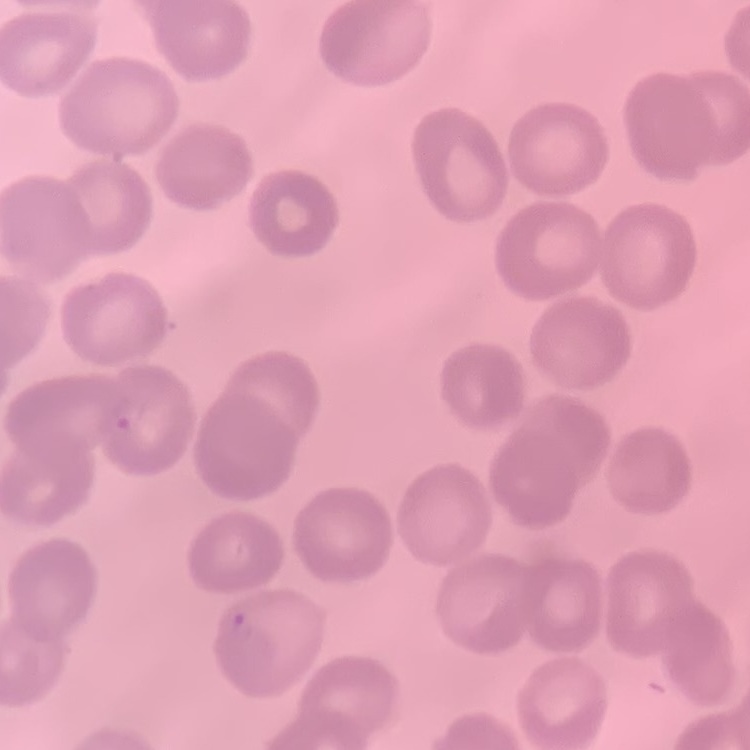

The erythrocytes exhibit no rouleaux formation. Thin peripheral smear. Field's or Giemsa stain. One tile cut from a larger photomicrograph.